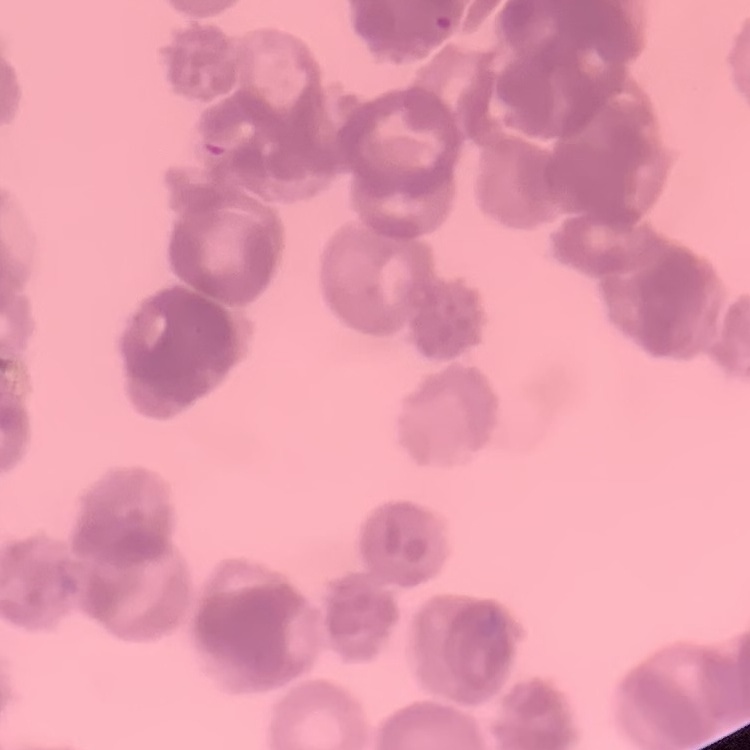
The erythrocytes show rouleaux formation. Square crop of a larger photomicrograph. Thin blood smear. Stained with either Field's or Giemsa.